Report the malaria status of this cell.
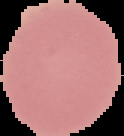

It is uninfected.

Summary:
  - Preparation: thin blood film
  - Image size: 124×136 pixels
  - Image type: segmented cell region with the area outside set to black